Assess the morphology of the red blood cells.
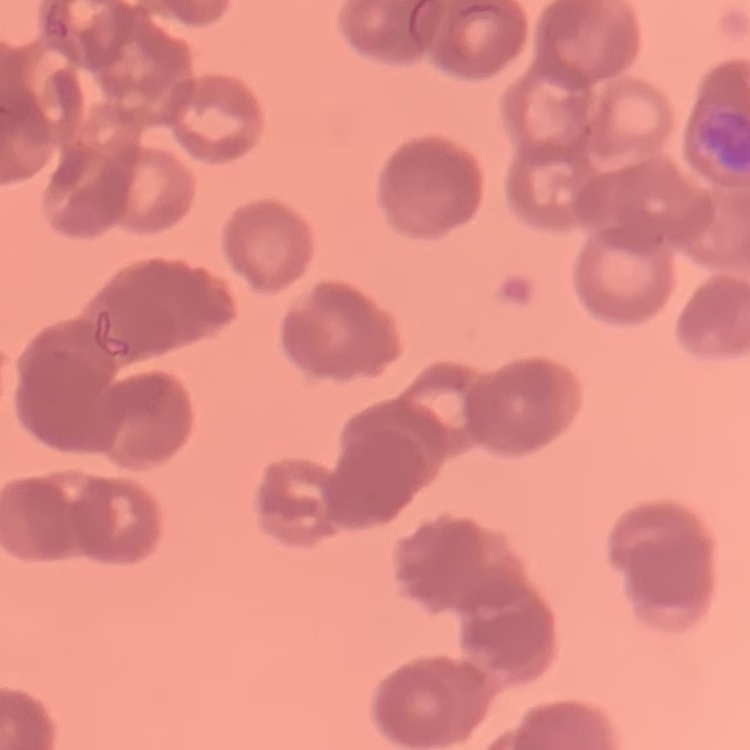

Rouleaux formation.

Summary:
  - Stain: Field's or Giemsa
  - Preparation: thin blood smear
  - Image type: one tile cut from a larger photomicrograph